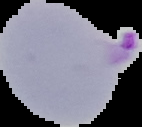
From a thin blood smear. Result: malaria parasites identified. Segmented cell region on a black background. Image is 142×127 pixels.